Identify the parasite.
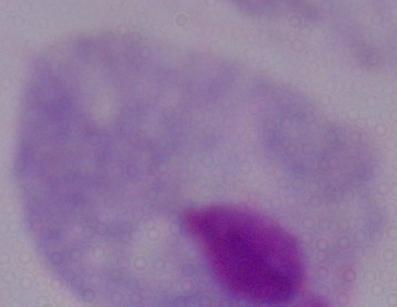
A trichomonad.

Photomicrograph. Captured at 1000x magnification.